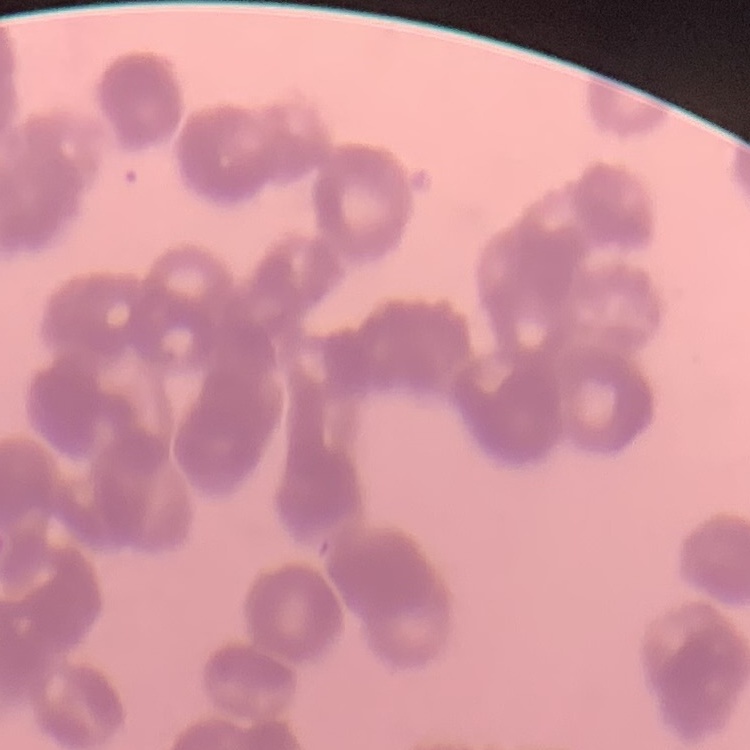

Summary:
  - Erythrocyte morphology: rouleaux formation
  - Image type: one tile cut from a larger photomicrograph
  - Stain: Field's or Giemsa
  - Preparation: thin peripheral smear